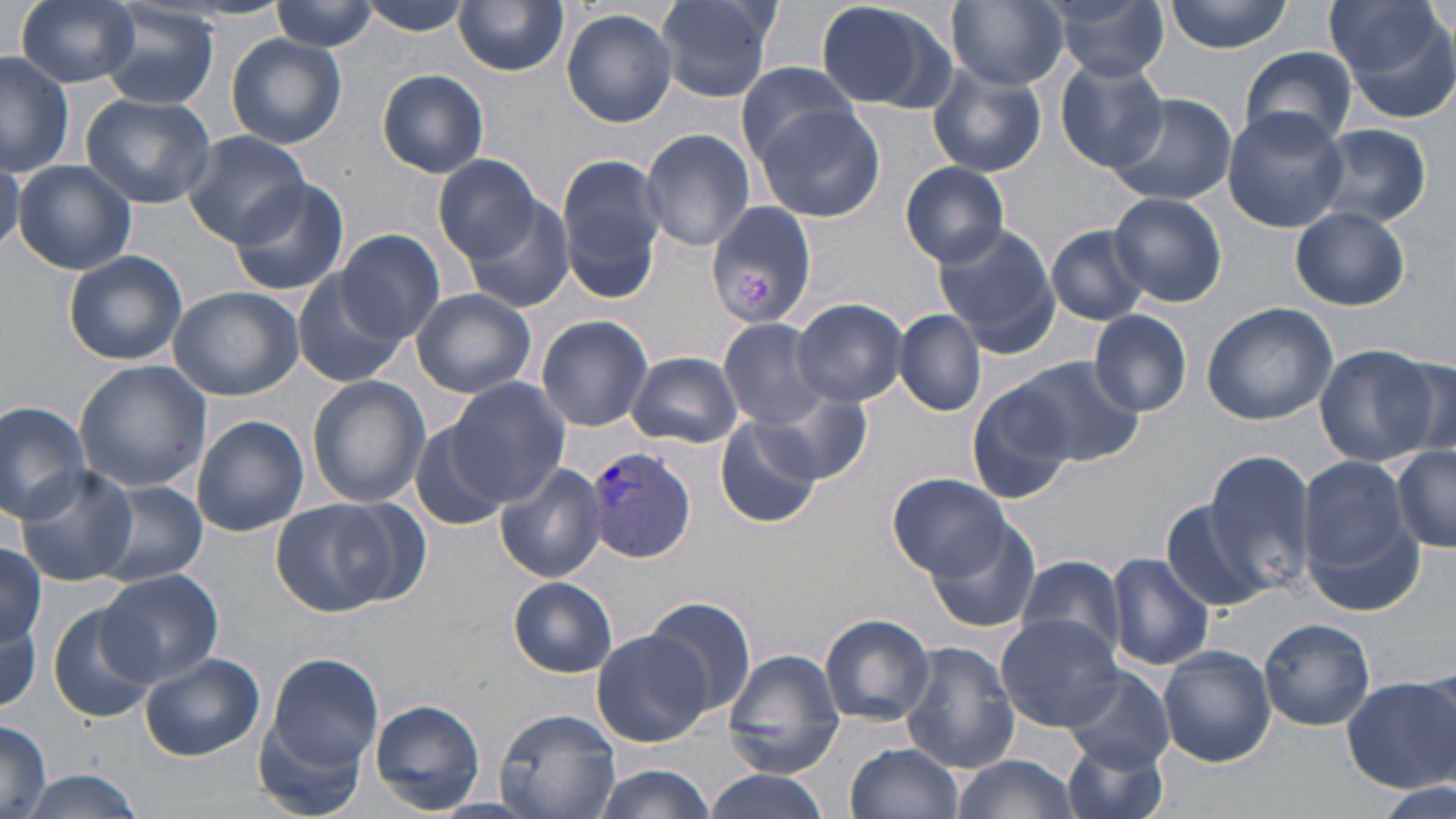
slide_level_diagnosis: Plasmodium vivax
uninfected_red_blood_cell_locations: 'approximate bounding boxes as named x1/y1/x2/y2 corners in pixels: (x1=13, y1=0, x2=141, y2=87), (x1=358, y1=0, x2=475, y2=38), (x1=656, y1=0, x2=778, y2=103), (x1=811, y1=0, x2=956, y2=113), (x1=948, y1=0, x2=1067, y2=90), (x1=1166, y1=0, x2=1292, y2=53), (x1=1323, y1=0, x2=1456, y2=109), (x1=271, y1=1, x2=378, y2=53), (x1=454, y1=1, x2=569, y2=76), (x1=1048, y1=2, x2=1168, y2=81), (x1=98, y1=6, x2=221, y2=111), (x1=562, y1=9, x2=679, y2=128), (x1=227, y1=35, x2=347, y2=148), (x1=210, y1=36, x2=337, y2=241), (x1=1240, y1=47, x2=1357, y2=148), (x1=0, y1=50, x2=76, y2=177), (x1=1056, y1=59, x2=1169, y2=173), (x1=736, y1=61, x2=862, y2=162), (x1=926, y1=65, x2=1047, y2=178), (x1=377, y1=69, x2=490, y2=179), (x1=80, y1=92, x2=217, y2=208), (x1=1105, y1=93, x2=1237, y2=207), (x1=753, y1=104, x2=885, y2=222), (x1=1222, y1=109, x2=1348, y2=231), (x1=1310, y1=124, x2=1432, y2=227), (x1=638, y1=129, x2=756, y2=250), (x1=181, y1=130, x2=310, y2=246), (x1=432, y1=153, x2=547, y2=263), (x1=557, y1=153, x2=666, y2=291), (x1=0, y1=160, x2=25, y2=254), (x1=13, y1=160, x2=137, y2=275), (x1=899, y1=161, x2=1010, y2=267), (x1=227, y1=176, x2=350, y2=295), (x1=1108, y1=192, x2=1228, y2=308), (x1=459, y1=194, x2=577, y2=314), (x1=201, y1=195, x2=331, y2=354), (x1=706, y1=202, x2=816, y2=329), (x1=1289, y1=205, x2=1411, y2=311), (x1=931, y1=222, x2=1062, y2=357), (x1=1044, y1=224, x2=1151, y2=326), (x1=335, y1=228, x2=446, y2=343), (x1=63, y1=250, x2=188, y2=365), (x1=292, y1=269, x2=410, y2=389), (x1=167, y1=286, x2=303, y2=400), (x1=409, y1=287, x2=538, y2=398), (x1=792, y1=297, x2=907, y2=406), (x1=1201, y1=301, x2=1339, y2=425), (x1=894, y1=309, x2=986, y2=417), (x1=1088, y1=309, x2=1193, y2=416), (x1=535, y1=314, x2=653, y2=431), (x1=715, y1=317, x2=832, y2=429), (x1=1314, y1=345, x2=1439, y2=466), (x1=626, y1=351, x2=743, y2=448), (x1=1386, y1=354, x2=1455, y2=462), (x1=1007, y1=357, x2=1144, y2=467), (x1=72, y1=359, x2=212, y2=495), (x1=307, y1=376, x2=431, y2=508), (x1=444, y1=377, x2=572, y2=504), (x1=963, y1=380, x2=1076, y2=501), (x1=762, y1=391, x2=871, y2=481), (x1=0, y1=401, x2=93, y2=523), (x1=713, y1=412, x2=826, y2=528), (x1=190, y1=415, x2=308, y2=537), (x1=411, y1=421, x2=511, y2=530), (x1=1390, y1=445, x2=1456, y2=554), (x1=1204, y1=448, x2=1318, y2=594), (x1=1296, y1=455, x2=1416, y2=593), (x1=494, y1=461, x2=608, y2=584), (x1=17, y1=465, x2=139, y2=585), (x1=885, y1=473, x2=1011, y2=580), (x1=98, y1=481, x2=207, y2=586), (x1=1158, y1=497, x2=1274, y2=615), (x1=270, y1=498, x2=405, y2=616), (x1=928, y1=521, x2=1043, y2=634), (x1=0, y1=543, x2=47, y2=647), (x1=1106, y1=550, x2=1214, y2=671), (x1=1014, y1=553, x2=1129, y2=666), (x1=98, y1=571, x2=224, y2=685), (x1=509, y1=579, x2=618, y2=677), (x1=643, y1=595, x2=757, y2=719), (x1=0, y1=602, x2=42, y2=713), (x1=46, y1=602, x2=156, y2=724), (x1=820, y1=613, x2=936, y2=725), (x1=995, y1=614, x2=1124, y2=733), (x1=1259, y1=618, x2=1376, y2=731), (x1=591, y1=630, x2=709, y2=747), (x1=900, y1=642, x2=1020, y2=773), (x1=1157, y1=646, x2=1276, y2=767), (x1=723, y1=650, x2=845, y2=777), (x1=140, y1=652, x2=264, y2=761), (x1=261, y1=652, x2=385, y2=781), (x1=1061, y1=665, x2=1175, y2=775), (x1=1341, y1=673, x2=1456, y2=793), (x1=369, y1=699, x2=486, y2=814), (x1=492, y1=706, x2=621, y2=819), (x1=256, y1=708, x2=373, y2=818), (x1=0, y1=721, x2=52, y2=817), (x1=1061, y1=736, x2=1171, y2=819), (x1=846, y1=741, x2=965, y2=819), (x1=947, y1=753, x2=1083, y2=819), (x1=586, y1=765, x2=716, y2=819), (x1=12, y1=771, x2=149, y2=819), (x1=704, y1=771, x2=838, y2=819), (x1=1379, y1=779, x2=1451, y2=819)'
modality: optical microscopy
platelet_locations: 'approximate bounding boxes as named x1/y1/x2/y2 corners in pixels: (x1=734, y1=273, x2=772, y2=310)'
field_of_view: single
preparation: thin blood film
magnification: 1000x
plasmodium_vivax_infected_red_blood_cell_locations: 'approximate bounding boxes as named x1/y1/x2/y2 corners in pixels: (x1=583, y1=444, x2=698, y2=565)'
stain: May-Grünwald-Giemsa
image_size: 1456×819 pixels